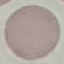
malaria status = uninfected
image type = cell patch, automatically extracted from a larger field of view and resized to 64 × 64 pixels
capture = smartphone camera at the microscope eyepiece
preparation = thin smear
stain = Giemsa